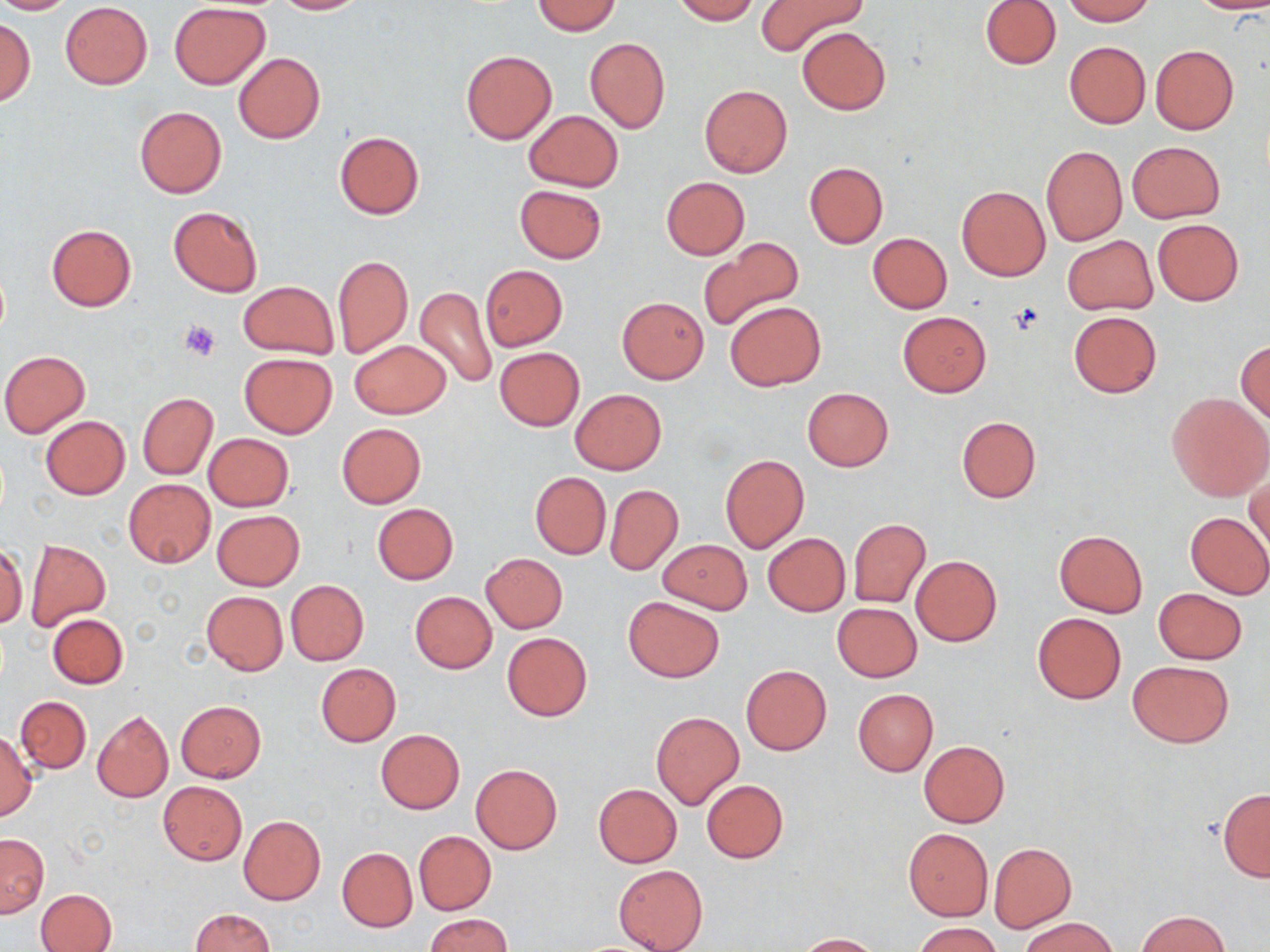
Approximate bounding boxes as [x1, y1, x2, y2] in pixels. Platelet locations: [179, 320, 220, 362]. Uninfected red blood cell locations: [0, 0, 75, 14], [272, 0, 369, 14], [672, 0, 760, 24], [981, 0, 1061, 69], [1063, 0, 1154, 25], [1189, 0, 1270, 14], [531, 1, 622, 35], [756, 1, 868, 57], [59, 2, 153, 89], [170, 3, 269, 88], [1, 18, 34, 105], [797, 26, 891, 115], [584, 36, 670, 133], [1064, 41, 1150, 128], [1151, 45, 1239, 135], [461, 50, 556, 144], [233, 53, 326, 144], [700, 84, 792, 177], [134, 106, 227, 198], [522, 110, 623, 192], [335, 131, 423, 219], [1127, 140, 1225, 223], [1041, 145, 1127, 245], [804, 162, 886, 248], [661, 177, 749, 259], [513, 184, 607, 262], [956, 185, 1051, 282], [168, 206, 263, 297], [1152, 219, 1244, 305], [46, 223, 137, 311], [868, 232, 952, 313], [1062, 235, 1157, 314], [698, 240, 806, 331], [332, 254, 412, 357], [481, 264, 568, 350], [238, 280, 339, 359], [415, 286, 498, 390], [616, 296, 708, 383], [725, 302, 825, 390], [1068, 310, 1161, 399], [898, 311, 992, 396], [349, 340, 451, 419], [1237, 340, 1270, 425], [495, 347, 585, 430], [0, 351, 90, 437], [239, 353, 337, 438], [802, 387, 892, 471], [570, 389, 667, 475], [1167, 391, 1269, 500], [138, 393, 217, 479], [41, 416, 130, 499], [956, 416, 1041, 502], [336, 423, 427, 509], [203, 433, 294, 511], [720, 455, 809, 552], [1247, 468, 1269, 555], [529, 471, 611, 559], [123, 479, 216, 568], [605, 483, 683, 574], [372, 503, 458, 585], [213, 510, 304, 590], [1184, 511, 1270, 599], [848, 518, 931, 607], [1054, 530, 1147, 616], [763, 533, 849, 615], [657, 538, 752, 614], [25, 540, 110, 631], [0, 545, 27, 628], [481, 553, 568, 633], [912, 555, 1002, 646], [287, 580, 369, 665], [1152, 587, 1249, 664], [201, 591, 288, 675], [409, 591, 497, 673], [623, 596, 725, 683], [832, 602, 922, 681], [1032, 612, 1126, 704], [48, 613, 127, 689], [502, 631, 593, 721], [1127, 659, 1235, 748], [315, 663, 401, 746], [741, 664, 831, 754], [853, 688, 938, 776], [16, 696, 91, 773], [175, 700, 267, 783], [91, 709, 174, 803], [651, 712, 745, 809], [376, 729, 464, 813], [0, 732, 37, 820], [918, 740, 1009, 827], [470, 764, 563, 854], [701, 780, 788, 863], [158, 782, 246, 865], [594, 784, 682, 867], [1217, 789, 1270, 881], [238, 814, 326, 906], [904, 828, 992, 920], [414, 830, 496, 915], [1, 834, 48, 917], [989, 843, 1075, 932], [338, 848, 417, 931], [613, 865, 709, 952], [38, 889, 117, 952], [190, 908, 273, 952], [1136, 911, 1229, 951], [425, 913, 514, 952], [1021, 916, 1120, 952], [913, 922, 1002, 952], [793, 933, 880, 951]. Slide-level diagnosis: negative for blood parasites. 1000x magnification. Light microscopy. Single field of view. Image is 1270×952 pixels. May-Grünwald-Giemsa-stained preparation. Thin blood film.